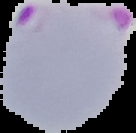 Result: Plasmodium parasites identified. The area outside the segmented cell region is set to black. Image is 136×133 pixels. From a thin blood smear.